Assess this cell for malaria.
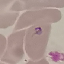
Parasitized.

Summary:
  - Image type: cell patch, automatically extracted from a larger field of view and resized to 64 × 64 pixels
  - Capture: smartphone through the microscope eyepiece
  - Stain: Giemsa
  - Preparation: thin smear